Identify the preparation type.
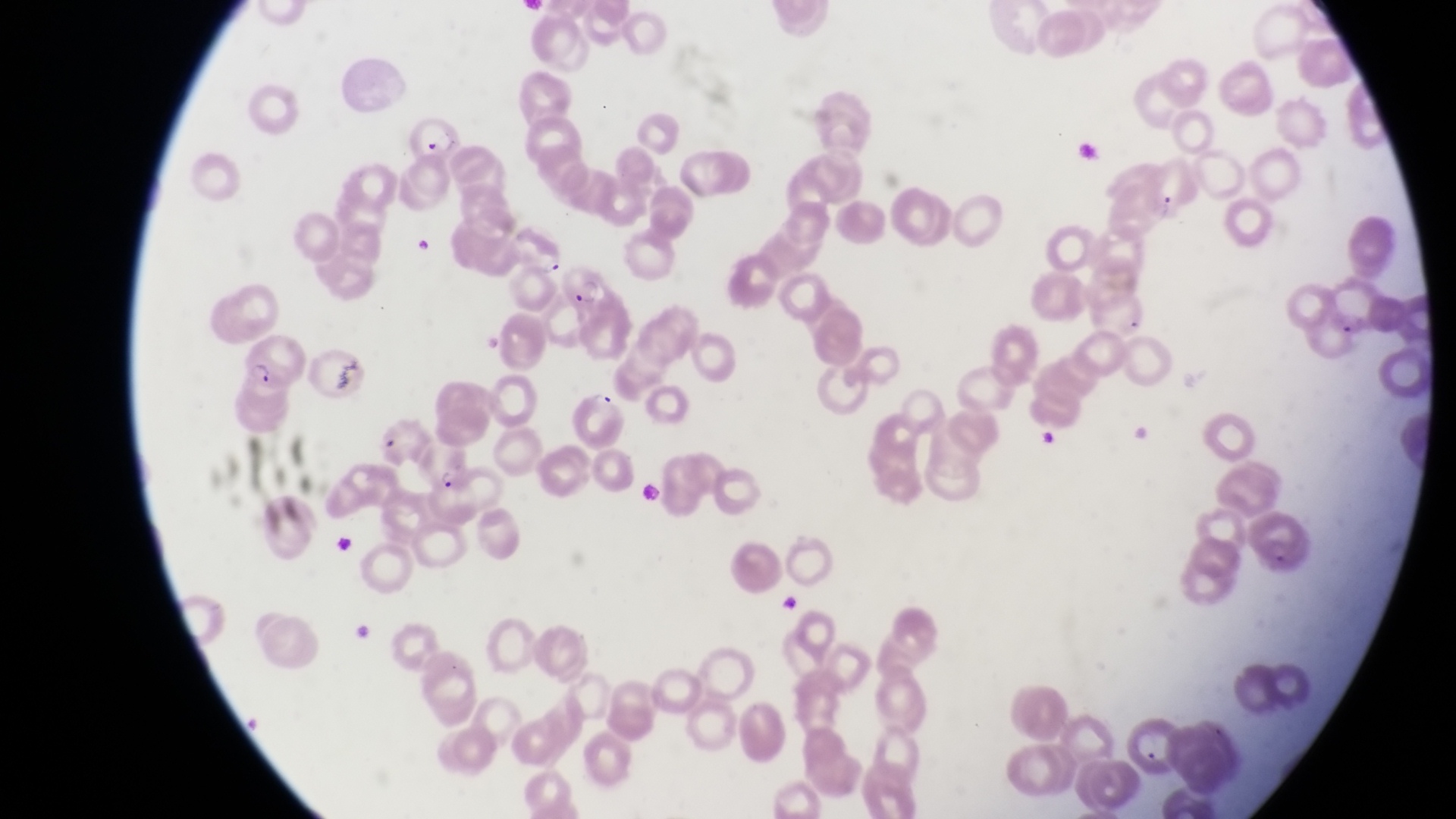

This is a thin smear.

Approximate bounding boxes as left top right bottom in pixels. Parasitised red blood cell locations: 412 116 462 162; 561 262 621 320; 238 334 302 393; 565 386 632 447; 377 415 432 467; 426 469 484 527; 1119 713 1178 773. Artifact (platelet-like body, stain precipitate, or debris) locations: 403 227 439 264; 1037 429 1069 453; 770 594 815 620. Sample from Uganda. Magnification of 1000x. Single field of view. Image is 1456×819 pixels. Captured by a smartphone held over the eyepiece of an Olympus CX-23 microscope.